Locate every parasitized red blood cell.
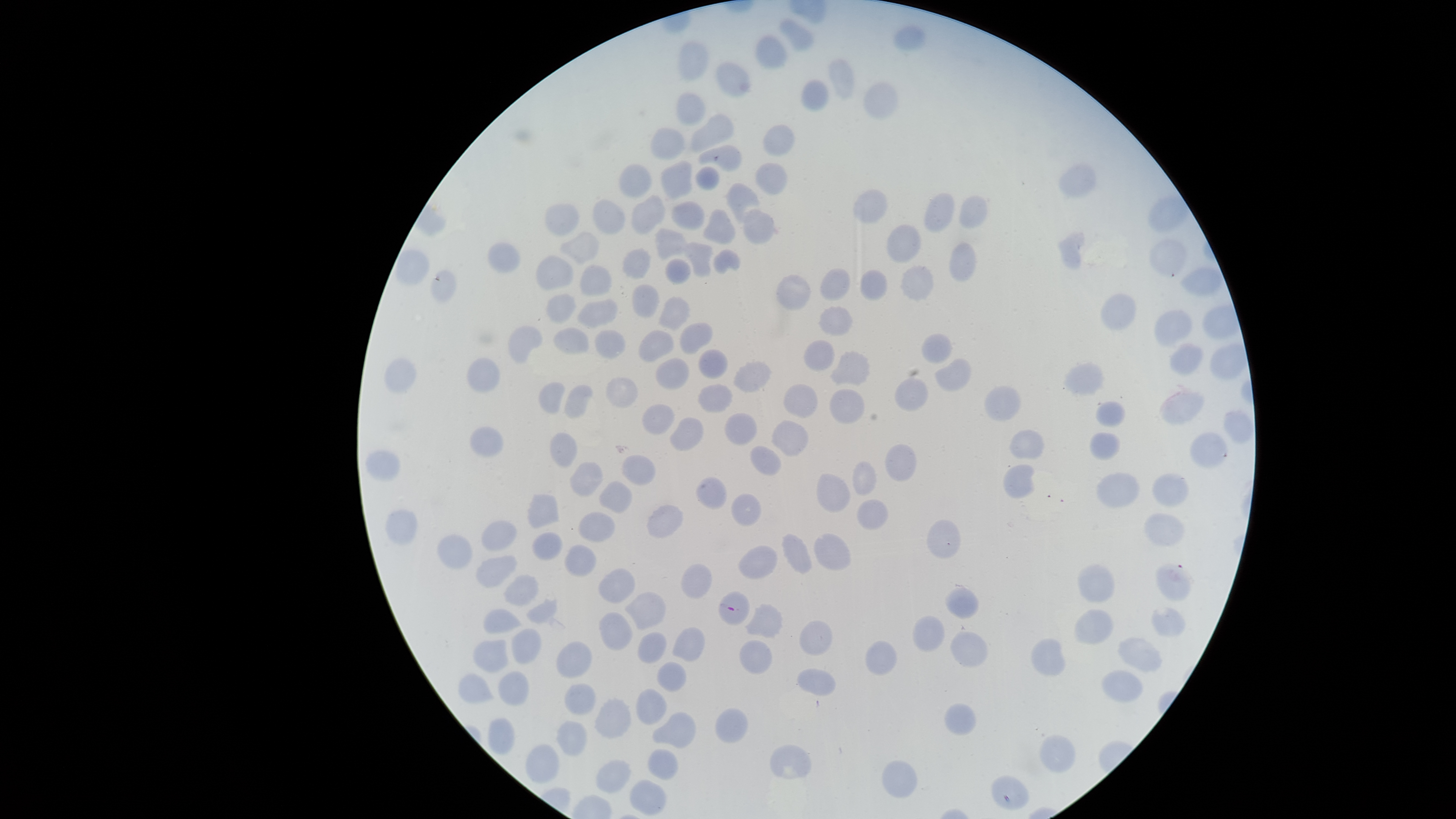

Approximate bounding boxes, in pixels from the top-left corner.
Parasitized red blood cells: (left=718, top=591, right=751, bottom=625).

preparation = thin blood film
uninfected red blood cells = approximate bounding boxes, in pixels from the top-left corner: (left=777, top=16, right=815, bottom=52), (left=893, top=24, right=928, bottom=51), (left=753, top=34, right=790, bottom=71), (left=678, top=42, right=709, bottom=81), (left=826, top=57, right=856, bottom=101), (left=715, top=61, right=753, bottom=98), (left=801, top=78, right=830, bottom=112), (left=864, top=81, right=900, bottom=120), (left=676, top=92, right=706, bottom=127), (left=690, top=113, right=734, bottom=153), (left=763, top=124, right=795, bottom=156), (left=650, top=128, right=685, bottom=161), (left=698, top=145, right=742, bottom=172), (left=659, top=158, right=694, bottom=200), (left=1056, top=161, right=1097, bottom=199), (left=755, top=162, right=789, bottom=195), (left=618, top=164, right=653, bottom=196), (left=695, top=166, right=721, bottom=189), (left=725, top=181, right=762, bottom=224), (left=853, top=188, right=887, bottom=223), (left=924, top=192, right=954, bottom=232), (left=631, top=195, right=667, bottom=234), (left=958, top=195, right=987, bottom=228), (left=1148, top=195, right=1189, bottom=233), (left=592, top=198, right=627, bottom=234), (left=671, top=201, right=705, bottom=229), (left=542, top=203, right=580, bottom=237), (left=743, top=207, right=776, bottom=244), (left=701, top=208, right=736, bottom=244), (left=886, top=223, right=922, bottom=263), (left=653, top=228, right=689, bottom=261), (left=560, top=230, right=600, bottom=265), (left=1055, top=231, right=1085, bottom=270), (left=1149, top=238, right=1186, bottom=278), (left=948, top=241, right=977, bottom=283), (left=487, top=242, right=520, bottom=273), (left=687, top=242, right=714, bottom=277), (left=622, top=248, right=652, bottom=278), (left=713, top=249, right=741, bottom=274), (left=534, top=255, right=574, bottom=291), (left=666, top=258, right=693, bottom=285), (left=578, top=264, right=613, bottom=296), (left=900, top=264, right=934, bottom=303), (left=860, top=267, right=889, bottom=301), (left=1179, top=267, right=1221, bottom=297), (left=430, top=268, right=457, bottom=303), (left=819, top=268, right=851, bottom=301), (left=775, top=274, right=812, bottom=311), (left=632, top=283, right=659, bottom=318), (left=1100, top=292, right=1137, bottom=329), (left=547, top=294, right=576, bottom=321), (left=576, top=297, right=618, bottom=329), (left=657, top=297, right=691, bottom=332), (left=817, top=305, right=853, bottom=336), (left=1154, top=310, right=1193, bottom=348), (left=679, top=322, right=712, bottom=356), (left=507, top=324, right=544, bottom=365), (left=553, top=325, right=590, bottom=354), (left=594, top=329, right=626, bottom=359), (left=638, top=330, right=674, bottom=363), (left=921, top=332, right=953, bottom=364), (left=803, top=339, right=834, bottom=372), (left=1169, top=344, right=1203, bottom=376), (left=698, top=347, right=729, bottom=379), (left=829, top=350, right=872, bottom=385), (left=385, top=357, right=417, bottom=393), (left=655, top=357, right=690, bottom=390), (left=465, top=358, right=501, bottom=393), (left=731, top=358, right=774, bottom=393), (left=934, top=358, right=971, bottom=390), (left=1062, top=361, right=1105, bottom=398), (left=605, top=375, right=639, bottom=409), (left=895, top=376, right=930, bottom=411), (left=539, top=382, right=565, bottom=414), (left=1158, top=383, right=1206, bottom=424), (left=697, top=384, right=733, bottom=413), (left=782, top=384, right=817, bottom=418), (left=563, top=385, right=594, bottom=420), (left=983, top=385, right=1022, bottom=421), (left=829, top=388, right=866, bottom=424), (left=1096, top=401, right=1126, bottom=427), (left=642, top=404, right=675, bottom=435), (left=724, top=412, right=759, bottom=446), (left=670, top=416, right=704, bottom=451), (left=770, top=419, right=809, bottom=457), (left=469, top=425, right=505, bottom=459), (left=1009, top=429, right=1046, bottom=459), (left=549, top=431, right=579, bottom=469), (left=1089, top=432, right=1121, bottom=461), (left=1189, top=432, right=1229, bottom=469), (left=885, top=444, right=917, bottom=482), (left=749, top=445, right=783, bottom=475), (left=365, top=449, right=402, bottom=482), (left=619, top=454, right=656, bottom=485), (left=852, top=460, right=878, bottom=497), (left=569, top=462, right=604, bottom=497), (left=1002, top=464, right=1036, bottom=498), (left=1096, top=472, right=1140, bottom=508), (left=1152, top=472, right=1190, bottom=507), (left=816, top=473, right=851, bottom=513), (left=695, top=477, right=728, bottom=510), (left=598, top=481, right=632, bottom=514), (left=731, top=492, right=762, bottom=526), (left=527, top=493, right=560, bottom=528), (left=856, top=499, right=889, bottom=531), (left=645, top=504, right=684, bottom=538), (left=385, top=510, right=418, bottom=547), (left=578, top=512, right=616, bottom=542), (left=1144, top=512, right=1185, bottom=547), (left=927, top=519, right=961, bottom=558), (left=481, top=520, right=517, bottom=550), (left=532, top=532, right=562, bottom=561), (left=436, top=533, right=474, bottom=570), (left=781, top=533, right=812, bottom=573), (left=813, top=533, right=851, bottom=570), (left=563, top=544, right=596, bottom=576), (left=737, top=545, right=778, bottom=579), (left=476, top=554, right=518, bottom=589), (left=681, top=562, right=713, bottom=599), (left=1077, top=563, right=1115, bottom=603), (left=1155, top=563, right=1193, bottom=602), (left=598, top=567, right=636, bottom=604), (left=503, top=574, right=539, bottom=607), (left=944, top=587, right=981, bottom=620), (left=625, top=591, right=666, bottom=630), (left=525, top=598, right=558, bottom=625), (left=744, top=603, right=785, bottom=639), (left=1151, top=606, right=1187, bottom=638), (left=482, top=608, right=524, bottom=634), (left=1074, top=609, right=1115, bottom=644), (left=599, top=611, right=634, bottom=650), (left=912, top=615, right=946, bottom=652), (left=799, top=620, right=833, bottom=656), (left=672, top=627, right=704, bottom=661), (left=511, top=628, right=543, bottom=664), (left=637, top=631, right=666, bottom=663), (left=950, top=631, right=989, bottom=668), (left=1118, top=636, right=1165, bottom=673), (left=1032, top=637, right=1065, bottom=675), (left=473, top=639, right=511, bottom=674), (left=738, top=640, right=773, bottom=674), (left=865, top=640, right=897, bottom=675), (left=556, top=641, right=592, bottom=677), (left=656, top=660, right=688, bottom=691), (left=796, top=668, right=836, bottom=696), (left=1102, top=669, right=1143, bottom=702), (left=498, top=671, right=530, bottom=706), (left=459, top=672, right=495, bottom=705), (left=565, top=683, right=596, bottom=715), (left=636, top=688, right=668, bottom=725), (left=593, top=698, right=632, bottom=739), (left=943, top=703, right=976, bottom=735), (left=715, top=708, right=749, bottom=743), (left=652, top=711, right=697, bottom=748), (left=486, top=718, right=515, bottom=755), (left=555, top=719, right=588, bottom=755), (left=1039, top=734, right=1076, bottom=771), (left=525, top=744, right=559, bottom=783), (left=769, top=744, right=813, bottom=780), (left=647, top=748, right=679, bottom=780), (left=596, top=759, right=633, bottom=793), (left=881, top=759, right=918, bottom=798), (left=990, top=775, right=1030, bottom=810), (left=629, top=778, right=668, bottom=815)
species = Plasmodium falciparum
field of view = single
capture = smartphone photograph through the microscope eyepiece
visible region = circular
image size = 1456×819 pixels
stain = Giemsa